Classify this cell by malaria status.
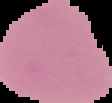
Uninfected.

{
  "preparation": "thin blood film",
  "image_size": "112×103 pixels",
  "image_type": "segmented cell region with the area outside set to black"
}